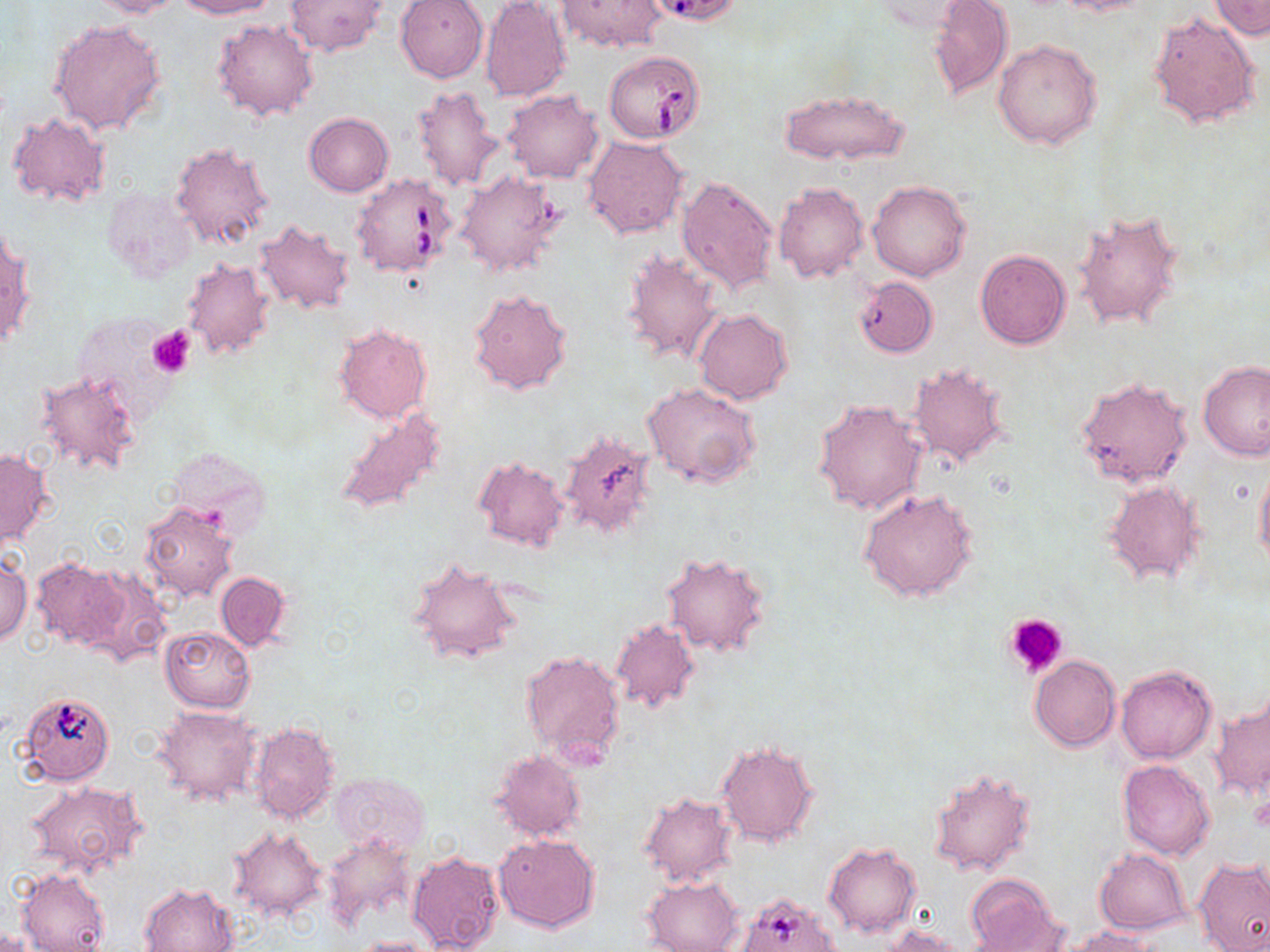
Approximate bounding boxes as [x1, y1, x2, y2] in pixels. Babesia divergens-infected red blood cell locations: [604, 50, 705, 143], [350, 172, 458, 278]. Platelet locations: [148, 326, 195, 378], [1002, 613, 1068, 679]. Uninfected red blood cell locations: [88, 0, 185, 19], [176, 0, 278, 18], [395, 0, 488, 83], [480, 0, 571, 103], [927, 0, 1013, 101], [1054, 0, 1157, 16], [284, 1, 388, 56], [556, 1, 668, 53], [1208, 1, 1269, 38], [868, 2, 973, 32], [1147, 11, 1261, 129], [49, 18, 167, 134], [211, 19, 318, 121], [993, 39, 1103, 150], [411, 84, 502, 190], [778, 88, 912, 165], [501, 89, 604, 183], [7, 112, 110, 208], [304, 113, 394, 196], [582, 135, 687, 240], [171, 141, 275, 254], [453, 170, 567, 277], [677, 174, 779, 293], [867, 180, 970, 282], [773, 181, 869, 284], [100, 184, 198, 282], [1072, 207, 1184, 331], [254, 218, 356, 315], [1, 230, 32, 355], [620, 248, 727, 365], [975, 249, 1071, 349], [182, 256, 277, 361], [854, 275, 938, 357], [467, 286, 572, 396], [694, 309, 793, 404], [117, 319, 199, 402], [335, 325, 431, 424], [1200, 360, 1269, 460], [908, 361, 1012, 467], [35, 370, 143, 476], [1077, 375, 1193, 488], [642, 383, 764, 491], [813, 398, 927, 514], [334, 407, 448, 517], [559, 429, 658, 540], [164, 447, 271, 537], [1, 448, 51, 548], [473, 457, 570, 550], [1254, 466, 1270, 569], [1102, 479, 1207, 585], [857, 487, 980, 603], [138, 500, 238, 604], [661, 551, 772, 657], [0, 552, 32, 646], [406, 556, 523, 666], [30, 558, 128, 649], [78, 565, 171, 667], [215, 571, 291, 651], [610, 618, 700, 714], [159, 626, 256, 712], [519, 648, 625, 766], [1030, 655, 1120, 751], [1115, 664, 1217, 764], [1211, 690, 1269, 800], [25, 693, 118, 785], [154, 706, 263, 806], [249, 720, 340, 825], [716, 739, 820, 847], [489, 751, 587, 841], [1117, 759, 1217, 861], [925, 763, 1036, 875], [329, 772, 431, 859], [28, 781, 145, 877], [639, 790, 738, 888], [228, 827, 327, 920], [320, 834, 418, 932], [494, 834, 600, 934], [823, 841, 921, 938], [1094, 849, 1191, 934], [406, 850, 503, 952], [1193, 859, 1270, 952], [16, 869, 111, 951], [965, 874, 1067, 951], [642, 876, 742, 952], [139, 882, 238, 952], [741, 892, 842, 952], [882, 924, 971, 951], [1065, 925, 1169, 951], [0, 926, 46, 952], [347, 936, 439, 951]. Slide-level diagnosis: Babesia divergens. Single field of view. Image is 1270×952 pixels. 1000x magnification. Thin blood film. Light microscopy. May-Grünwald-Giemsa stain.